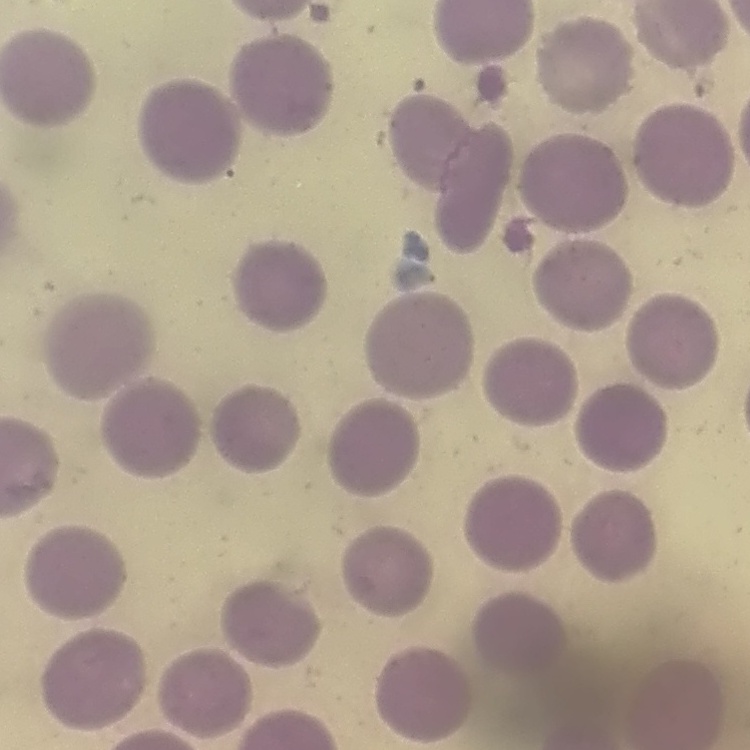

Summary:
  - Red blood cell morphology: no rouleaux formation
  - Image type: square crop of a larger photomicrograph
  - Stain: Field's or Giemsa
  - Preparation: thin blood smear